State which cell type is depicted.
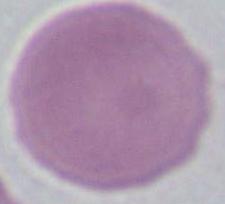

An erythrocyte.

{
  "magnification": "1000x",
  "modality": "micrograph"
}